Locate cells.
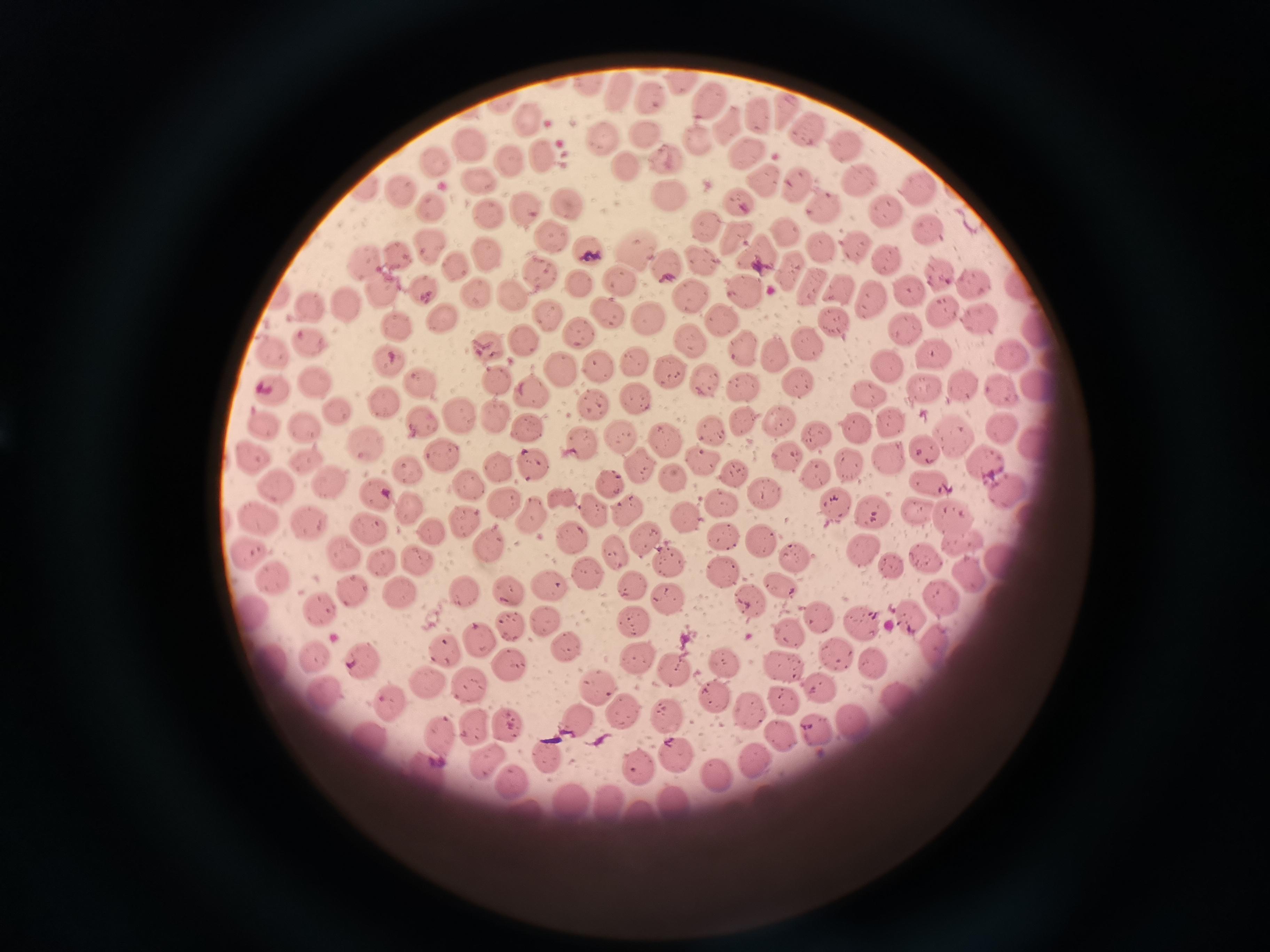

Approximate centers as [x, y] in pixels.
Cells: [678, 82], [617, 97], [651, 98], [709, 98], [785, 111], [760, 115], [525, 117], [728, 126], [806, 130], [646, 135], [604, 137], [697, 139], [850, 144], [470, 145], [744, 150], [669, 154], [543, 156], [436, 161], [509, 162], [626, 163], [857, 180], [760, 181], [479, 184], [795, 186], [362, 187], [921, 188], [667, 193], [399, 194], [739, 200], [563, 201], [428, 206], [824, 208], [525, 210], [885, 213], [485, 215], [705, 223], [785, 231], [924, 231], [552, 237], [736, 237], [429, 245], [857, 245], [634, 248], [823, 249], [592, 250], [398, 254], [758, 254], [484, 255], [701, 255], [884, 257], [366, 261], [455, 262], [667, 265], [790, 269], [938, 272], [540, 273], [619, 278], [584, 281], [973, 284], [1017, 284], [424, 286], [379, 287], [747, 287], [908, 288], [842, 289], [472, 292], [689, 296], [868, 296], [510, 298], [346, 304], [308, 307], [608, 311], [940, 313], [546, 314], [437, 316], [649, 317], [977, 318], [831, 319], [720, 320], [903, 321], [398, 327], [578, 329], [1034, 329], [525, 336], [308, 341], [810, 341], [689, 342], [741, 347], [928, 349], [774, 351], [272, 353], [1010, 353], [632, 361], [391, 364], [598, 365], [885, 366], [562, 367], [669, 370], [421, 379], [496, 379], [311, 380], [706, 380], [800, 381], [1035, 381], [961, 384], [744, 386], [923, 388], [531, 389], [272, 391], [871, 392], [998, 392], [594, 397], [635, 398], [384, 404], [336, 409], [495, 412], [460, 414], [422, 418], [888, 419], [742, 421], [778, 421], [263, 426], [529, 426], [304, 427], [712, 430], [855, 430], [999, 430], [618, 435], [816, 436], [953, 438], [583, 439], [666, 440], [1034, 441], [360, 443], [922, 450], [442, 452], [889, 456], [786, 458], [252, 459], [534, 460], [306, 461], [700, 461], [638, 462], [851, 463], [983, 464], [497, 466], [410, 470], [817, 473], [736, 474], [675, 477], [931, 480], [609, 482], [472, 484], [331, 486], [1005, 487], [276, 488], [764, 492], [376, 495], [500, 498], [560, 499], [720, 502], [409, 505], [835, 506], [624, 507], [951, 509], [592, 510], [871, 511], [917, 511], [532, 513], [684, 516], [260, 519], [466, 522], [311, 525], [368, 525], [431, 529], [571, 533], [722, 535], [643, 537], [759, 539], [963, 539], [490, 544], [617, 551], [858, 552], [345, 553], [249, 555], [419, 557], [667, 557], [795, 558], [924, 558], [1000, 561], [382, 563], [888, 564], [721, 570], [588, 573], [968, 575], [276, 579], [629, 584], [549, 586], [509, 588], [465, 589], [354, 593], [401, 594], [940, 595], [663, 599], [751, 600], [317, 606], [815, 614], [909, 616], [633, 619], [545, 621], [858, 621], [511, 626], [787, 631], [475, 635], [565, 642], [933, 645], [447, 649], [836, 654], [318, 658], [722, 658], [633, 659], [360, 661], [875, 661], [783, 664], [509, 665], [671, 669], [427, 680], [471, 684], [595, 684], [818, 684], [322, 692], [713, 698], [784, 698], [895, 701], [388, 705], [749, 708], [622, 710], [667, 712], [850, 719], [573, 720], [508, 722], [478, 726], [816, 729], [782, 738], [371, 739], [444, 739], [547, 752], [672, 752], [752, 761], [482, 762], [637, 763], [431, 773], [714, 773], [516, 785], [573, 800], [673, 804], [610, 805], [646, 816].

stain = Giemsa
preparation = thin smear
field of view = single
image size = 1270×952 pixels
capture = smartphone through the microscope eyepiece